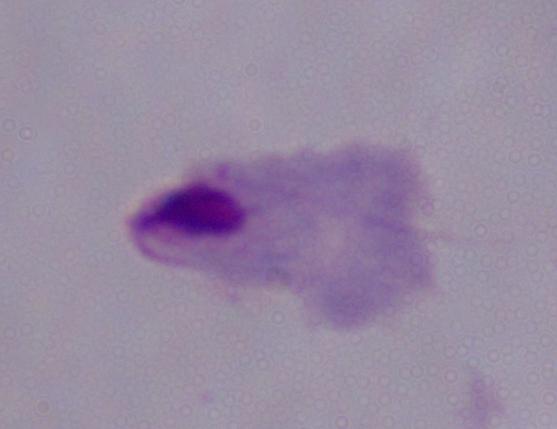
Summary:
  - Magnification: 1000x
  - Identification: trichomonad
  - Modality: photomicrograph